Outline each blood parasite and name the species.
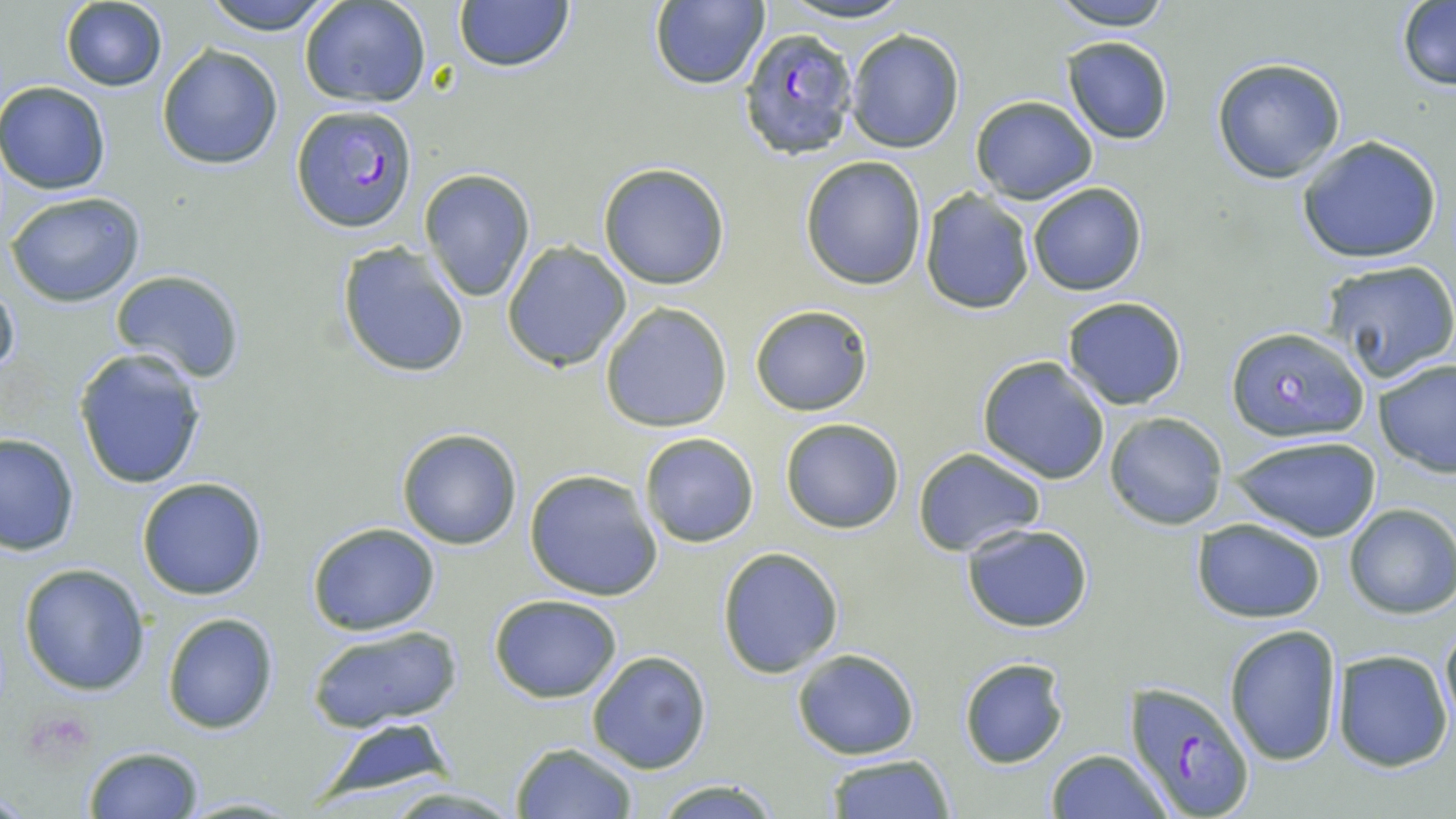

Approximate bounding boxes as (x1,y1)-(x2,y2) corner pairs in pixels.
Plasmodium falciparum-infected red blood cells: (736,27)-(863,164), (291,104)-(420,235), (1126,682)-(1255,815).
No Plasmodium ovale, Plasmodium malariae, Plasmodium vivax, Babesia divergens, or Trypanosoma brucei observed.

Uninfected red blood cell locations: (202,0)-(337,35), (300,0)-(432,109), (451,0)-(577,74), (1047,0)-(1178,30), (60,1)-(167,91), (647,1)-(771,89), (1395,2)-(1456,89), (846,28)-(964,153), (1061,35)-(1174,145), (157,44)-(283,169), (1211,56)-(1347,184), (977,71)-(1169,190), (0,81)-(111,195), (970,96)-(1096,203), (1294,134)-(1445,264), (800,155)-(927,290), (597,162)-(732,289), (419,168)-(537,302), (1027,182)-(1147,297), (6,190)-(146,307), (919,191)-(1036,315), (501,240)-(633,371), (336,242)-(472,380), (1320,258)-(1456,383), (108,271)-(247,386), (0,278)-(19,381), (1060,296)-(1189,409), (599,302)-(733,433), (750,303)-(875,417), (1226,327)-(1371,444), (71,347)-(209,490), (976,355)-(1111,485), (1374,358)-(1456,476), (1105,411)-(1228,530), (779,418)-(906,533), (396,427)-(524,551), (638,431)-(761,548), (0,433)-(78,557), (1229,434)-(1381,542), (912,447)-(1046,557), (524,468)-(664,601), (136,475)-(269,602), (1342,502)-(1456,620), (1191,517)-(1326,624), (307,522)-(441,636), (960,524)-(1095,633), (717,547)-(845,678), (18,563)-(152,696), (488,594)-(624,702), (161,610)-(279,733), (1439,614)-(1455,736), (1223,623)-(1343,766), (305,625)-(462,733), (534,626)-(670,774), (791,647)-(920,759), (1332,649)-(1454,773), (586,650)-(712,773), (958,656)-(1069,769), (308,720)-(458,804), (511,742)-(638,818), (80,746)-(206,819), (1047,749)-(1171,819), (822,752)-(956,819), (650,779)-(785,817), (379,785)-(526,818), (175,795)-(307,817). Slide-level diagnosis: Plasmodium falciparum. Thin blood film. Image is 1456×819 pixels. 1000x magnification. Optical microscopy. Single field of view. May-Grünwald-Giemsa-stained preparation.